Classify the preparation.
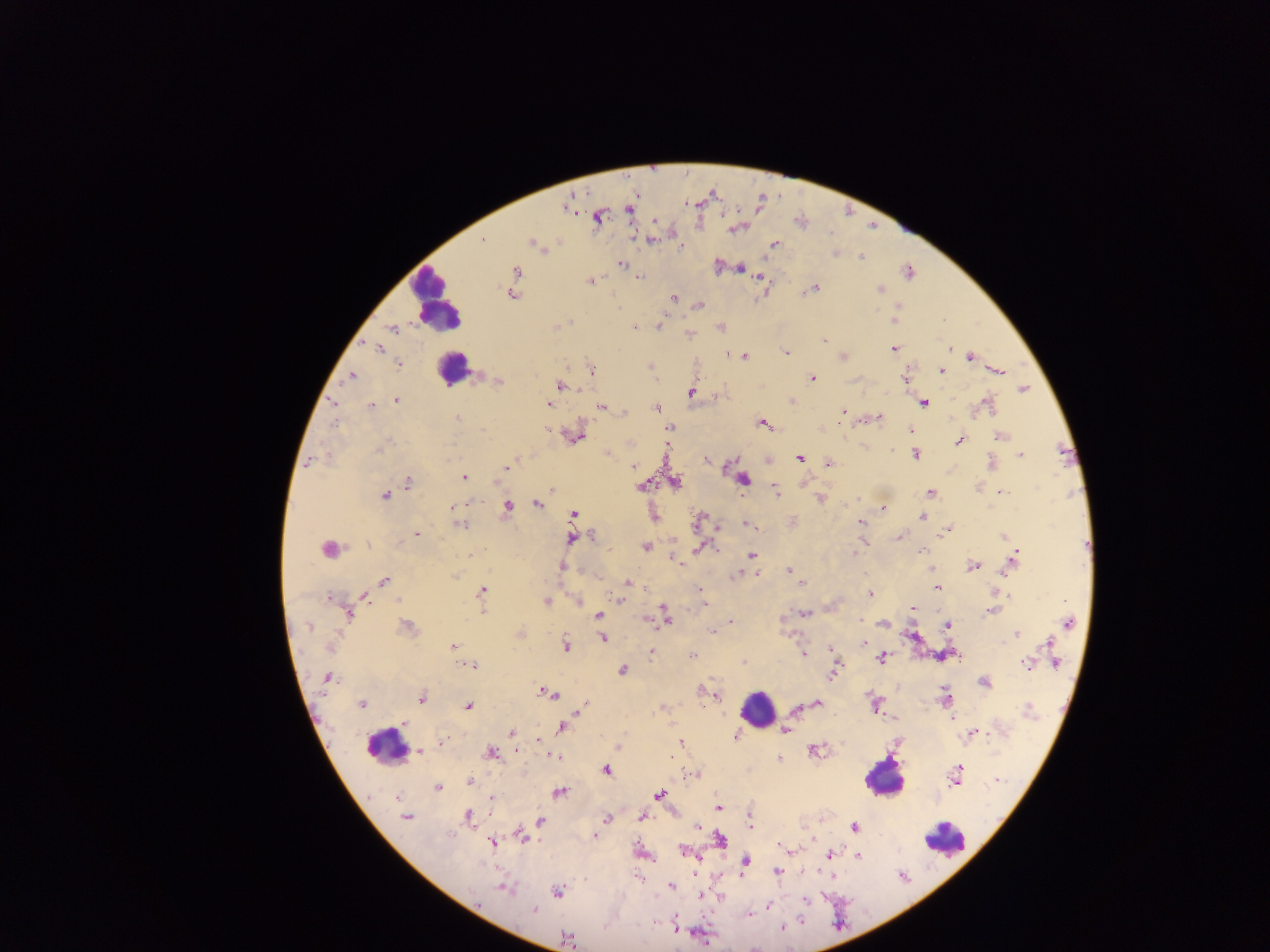
This is a thick smear.

Approximate centers as x y in pixels. Leukocyte locations: 438 300; 453 369; 756 710; 383 751; 884 779; 946 841. Malaria parasite locations: 629 210; 598 218; 655 221; 482 240; 532 242; 774 244; 681 246; 836 254; 861 257; 621 264; 740 268; 517 271; 909 272; 639 277; 760 278; 590 281; 810 290; 880 290; 512 295; 673 299; 699 305; 894 321; 659 326; 557 327; 635 327; 391 328; 688 334; 824 340; 949 348; 377 349; 894 349; 787 352; 744 356; 843 357; 971 357; 398 364; 652 368; 591 370; 941 371; 999 372; 351 376; 812 378; 498 381; 560 386; 1023 389; 691 393; 397 401; 790 401; 332 402; 924 403; 548 404; 987 404; 371 406; 601 407; 656 408; 843 411; 625 412; 879 417; 458 418; 334 424; 763 424; 669 428; 911 429; 483 430; 549 430; 1000 436; 577 437; 959 442; 379 449; 606 453; 915 455; 1020 455; 800 458; 706 460; 309 462; 829 463; 991 464; 633 466; 507 467; 464 477; 743 480; 408 482; 674 482; 641 486; 551 489; 775 491; 931 492; 1003 492; 385 495; 820 498; 537 504; 453 508; 507 508; 883 508; 573 514; 922 516; 699 520; 793 520; 860 522; 461 525; 748 525; 947 529; 416 534; 592 536; 1003 536; 900 537; 571 539; 367 545; 645 547; 328 548; 700 548; 856 549; 921 551; 854 553; 470 555; 751 555; 1014 559; 680 563; 972 566; 562 567; 788 571; 736 574; 757 574; 455 575; 385 580; 628 582; 801 583; 937 588; 482 590; 701 591; 870 594; 1009 595; 364 597; 330 599; 619 600; 545 602; 577 602; 703 604; 913 608; 483 611; 991 611; 805 613; 348 614; 599 616; 665 616; 646 620; 861 620; 732 621; 1069 623; 883 624; 947 626; 309 627; 406 630; 718 630; 713 631; 1016 633; 603 638; 864 643; 1049 644; 566 645; 453 646; 331 647; 831 650; 651 653; 803 654; 692 656; 882 657; 744 663; 1055 663; 1026 664; 473 666; 622 671; 835 672; 329 679; 984 683; 702 691; 549 693; 715 695; 946 697; 421 699; 362 704; 584 704; 816 704; 874 704; 468 706; 795 709; 658 710; 1027 710; 951 717; 404 723; 561 728; 785 731; 974 732; 513 733; 735 736; 539 740; 442 741; 681 744; 619 747; 815 750; 419 751; 517 751; 490 754; 554 756; 780 759; 606 770; 695 774; 955 776; 998 779; 470 781; 437 787; 559 793; 659 795; 397 797; 491 798; 717 807; 468 815; 406 817; 642 817; 607 818; 539 821; 749 823; 696 826; 854 827; 596 836; 522 838; 721 840; 492 843; 782 847; 684 851; 830 855; 859 855; 745 862; 776 871; 671 887; 504 888; 559 891; 700 895; 805 900; 768 906; 534 910; 750 914; 800 921; 781 928; 677 931; 568 939. Single field of view. Photographed through a microscope with a mobile-phone camera. Collected in Ghana. Image is 1270×952 pixels.